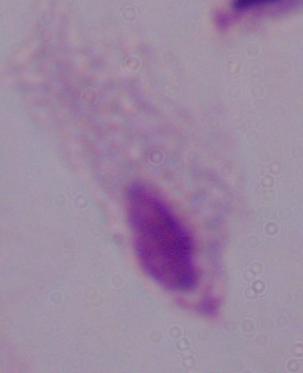
identification: trichomonad
modality: photomicrograph
magnification: 1000x